Comment on the morphology of the red blood cells.
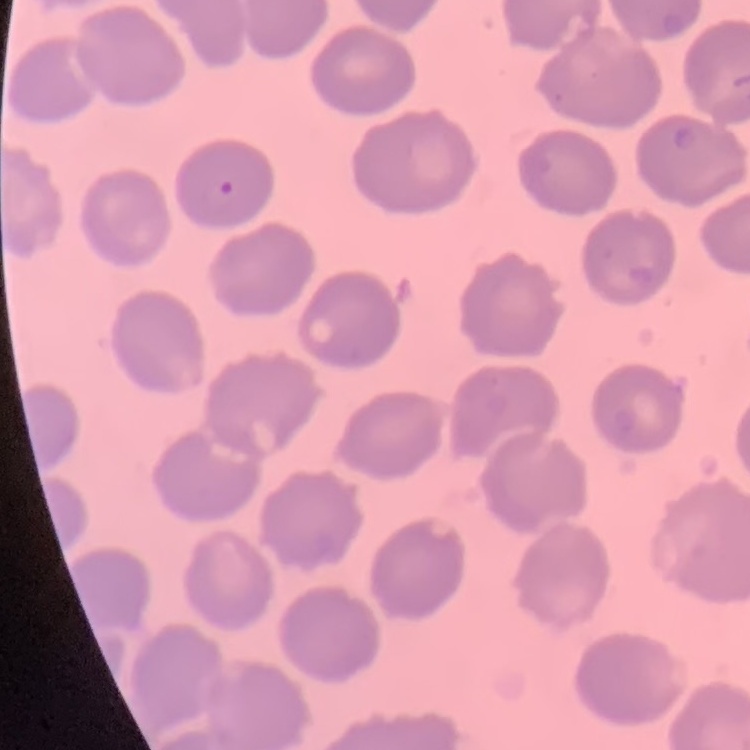

They show no rouleaux formation.

Summary:
  - Stain: Field's or Giemsa
  - Image type: square crop of a larger photomicrograph
  - Preparation: thin peripheral smear